Identify the parasite.
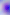

This is Toxoplasma gondii.

magnification = 400x
modality = micrograph